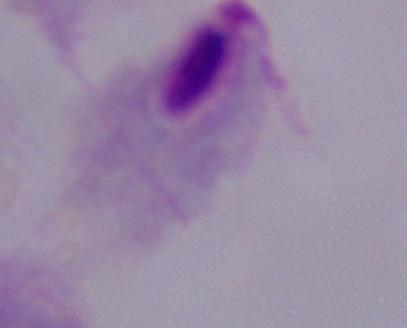
Summary:
  - Magnification: 1000x
  - Identification: trichomonad
  - Modality: photomicrograph